Comment on the morphology of the erythrocytes.
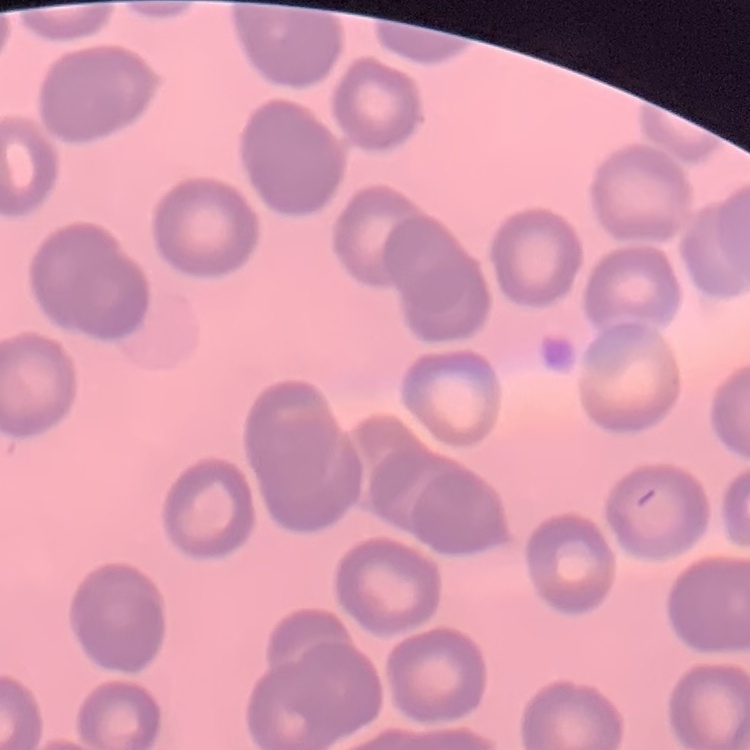
No rouleaux formation.

Field's or Giemsa stain. Thin peripheral smear. Square crop of a larger photomicrograph.